State the blood parasite species.
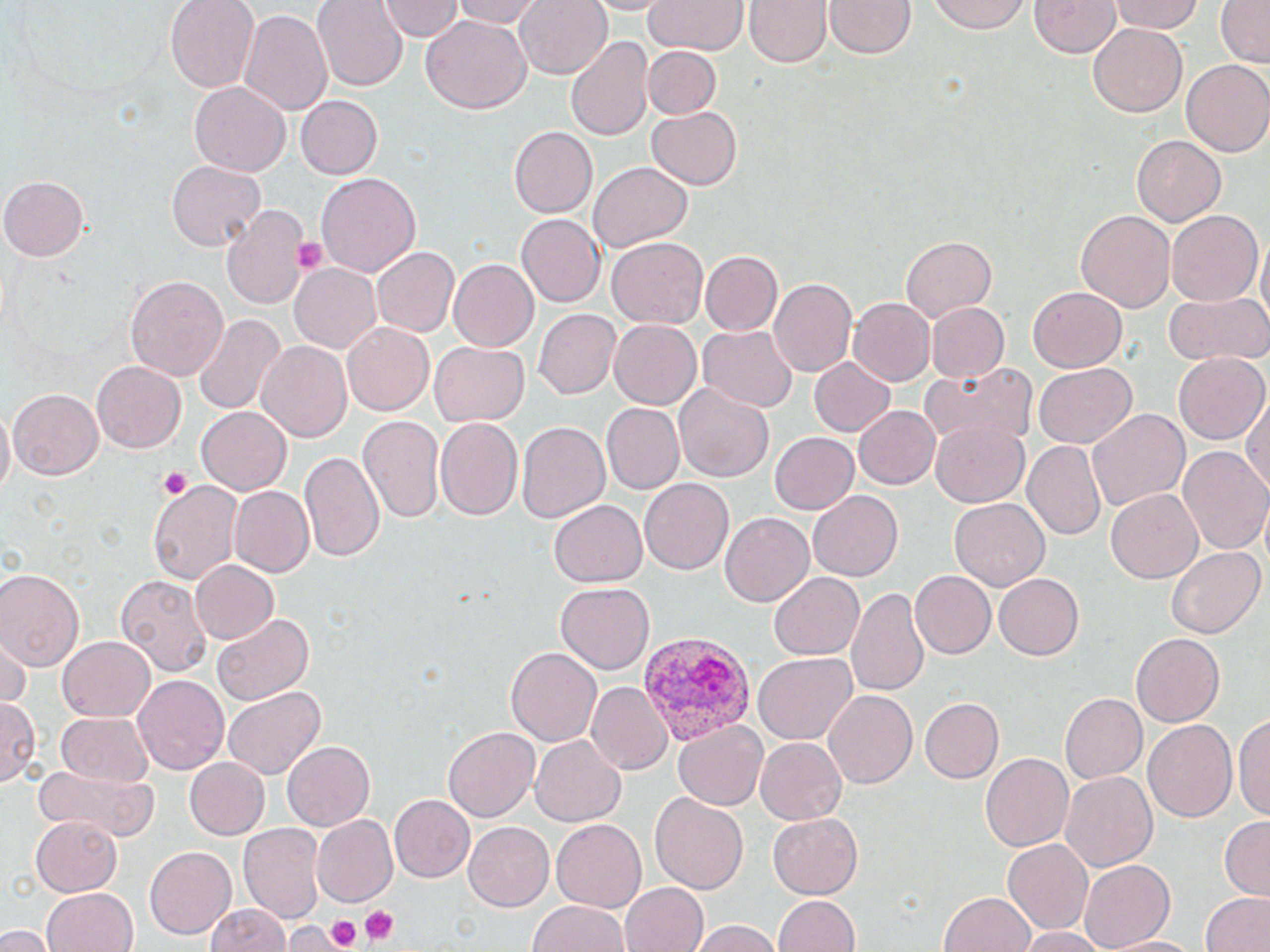

Plasmodium vivax.

{
  "image_size": "1270×952 pixels",
  "preparation": "thin blood film",
  "field_of_view": "single",
  "uninfected_red_blood_cell_locations": "approximate bounding boxes as [x1, y1, x2, y2] in pixels: [166, 0, 260, 93], [313, 0, 406, 91], [452, 0, 547, 29], [513, 0, 611, 80], [579, 0, 677, 15], [642, 0, 749, 55], [744, 0, 829, 70], [930, 0, 1028, 34], [1029, 0, 1119, 59], [1111, 0, 1203, 35], [1214, 0, 1270, 69], [378, 1, 464, 42], [826, 1, 914, 58], [238, 7, 333, 114], [532, 7, 656, 107], [423, 15, 531, 115], [1088, 27, 1183, 117], [565, 34, 655, 145], [644, 46, 721, 118], [1182, 60, 1270, 157], [190, 80, 293, 176], [295, 95, 383, 180], [645, 107, 741, 190], [508, 127, 596, 217], [1132, 136, 1226, 227], [167, 161, 263, 250], [588, 161, 693, 250], [315, 173, 421, 278], [3, 176, 90, 262], [220, 205, 309, 308], [1076, 208, 1177, 313], [1166, 211, 1262, 305], [517, 215, 605, 308], [898, 236, 995, 323], [607, 238, 708, 330], [372, 246, 460, 338], [701, 251, 782, 335], [449, 258, 540, 352], [290, 262, 383, 355], [125, 275, 227, 383], [769, 278, 856, 376], [1026, 288, 1128, 373], [1162, 292, 1268, 366], [848, 297, 935, 387], [925, 302, 1008, 384], [533, 308, 620, 399], [191, 314, 285, 418], [609, 319, 701, 409], [343, 322, 434, 415], [698, 326, 798, 412], [429, 341, 531, 426], [259, 342, 353, 444], [1172, 353, 1267, 443], [807, 355, 897, 438], [92, 362, 186, 454], [922, 362, 1039, 449], [1033, 364, 1135, 449], [673, 384, 775, 484], [8, 389, 105, 479], [1247, 398, 1270, 500], [0, 403, 15, 503], [601, 403, 684, 494], [853, 405, 940, 489], [197, 406, 292, 496], [1086, 406, 1190, 512], [359, 417, 445, 526], [436, 418, 522, 520], [515, 421, 609, 526], [929, 423, 1027, 505], [769, 431, 860, 515], [1023, 442, 1106, 539], [1178, 446, 1270, 558], [299, 452, 385, 564], [148, 477, 246, 589], [640, 478, 734, 575], [232, 486, 314, 578], [1105, 488, 1202, 584], [806, 490, 903, 581], [950, 497, 1051, 590], [549, 498, 648, 586], [720, 512, 815, 607], [1167, 545, 1265, 638], [188, 558, 278, 645], [0, 567, 84, 671], [911, 570, 999, 658], [768, 571, 864, 661], [993, 571, 1083, 658], [115, 572, 210, 677], [555, 582, 654, 675], [846, 586, 931, 698], [210, 613, 309, 705], [1131, 633, 1225, 726], [1, 637, 32, 709], [57, 638, 154, 723], [506, 648, 602, 746], [756, 653, 857, 744], [134, 675, 229, 779], [585, 682, 672, 775], [223, 687, 325, 778], [823, 690, 917, 789], [1059, 692, 1146, 785], [1, 697, 40, 788], [918, 697, 1003, 784], [57, 712, 154, 786], [1234, 712, 1270, 823], [1145, 719, 1238, 822], [674, 720, 768, 809], [443, 726, 537, 822], [531, 737, 625, 825], [757, 739, 846, 824], [280, 741, 374, 830], [979, 753, 1073, 852], [184, 758, 271, 840], [33, 762, 161, 841], [1059, 771, 1158, 871], [390, 794, 476, 882], [650, 794, 749, 895], [769, 812, 864, 899], [29, 815, 120, 897], [312, 815, 398, 905], [1220, 817, 1269, 897], [550, 820, 647, 912], [466, 821, 557, 910], [240, 825, 324, 923], [1003, 838, 1093, 932], [144, 845, 239, 939], [1077, 859, 1177, 949], [622, 880, 708, 952], [41, 886, 137, 952], [1203, 891, 1270, 952], [941, 892, 1038, 952], [773, 893, 859, 952], [527, 898, 631, 952], [204, 901, 293, 952], [688, 918, 784, 952], [284, 920, 340, 952], [0, 925, 51, 952], [1015, 926, 1110, 952], [1107, 934, 1205, 952]",
  "platelet_locations": "approximate bounding boxes as [x1, y1, x2, y2] in pixels: [292, 235, 331, 276], [157, 466, 191, 501], [359, 904, 401, 945], [319, 910, 363, 949]",
  "modality": "optical microscopy",
  "plasmodium_vivax_infected_red_blood_cell_locations": "approximate bounding boxes as [x1, y1, x2, y2] in pixels: [640, 633, 754, 747]",
  "stain": "May-Grünwald-Giemsa",
  "magnification": "1000x"
}